Locate every Plasmodium falciparum-infected red blood cell.
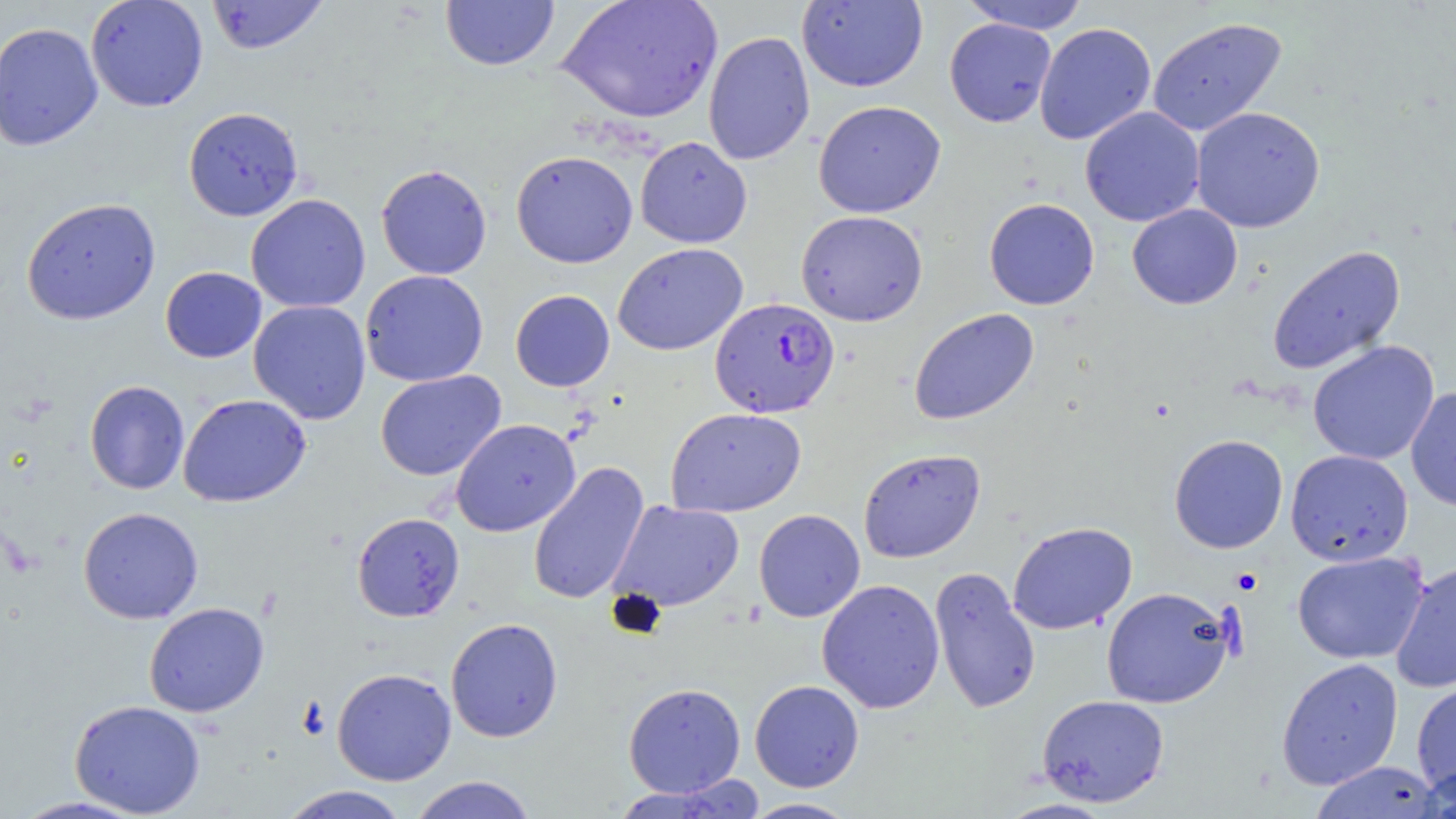
Approximate bounding boxes as [x1, y1, x2, y2] in pixels.
Plasmodium falciparum-infected red blood cells: [710, 297, 840, 418].

{
  "slide_level_diagnosis": "Plasmodium falciparum",
  "modality": "light microscopy",
  "stain": "May-Grünwald-Giemsa",
  "uninfected_red_blood_cell_locations": "approximate bounding boxes as [x1, y1, x2, y2] in pixels: [85, 0, 209, 112], [206, 0, 330, 55], [440, 0, 560, 71], [557, 0, 723, 124], [797, 1, 928, 92], [959, 1, 1090, 34], [1147, 16, 1288, 137], [944, 18, 1056, 128], [1, 22, 103, 151], [1034, 22, 1156, 145], [703, 30, 815, 166], [813, 100, 946, 218], [1190, 106, 1326, 233], [183, 107, 304, 221], [1079, 107, 1205, 227], [635, 136, 752, 248], [511, 150, 638, 268], [376, 164, 492, 279], [245, 194, 371, 313], [21, 197, 161, 325], [984, 198, 1100, 310], [1127, 204, 1243, 310], [795, 210, 928, 326], [613, 243, 748, 356], [1266, 244, 1405, 375], [160, 266, 266, 363], [360, 269, 488, 387], [510, 289, 615, 392], [248, 300, 371, 425], [908, 308, 1039, 425], [1307, 340, 1440, 465], [375, 369, 506, 481], [84, 380, 190, 495], [1406, 387, 1456, 512], [178, 393, 311, 507], [665, 407, 807, 517], [450, 418, 580, 537], [1169, 434, 1288, 553], [858, 448, 986, 563], [1285, 449, 1414, 566], [528, 461, 650, 606], [608, 500, 744, 612], [78, 506, 204, 624], [753, 509, 866, 622], [352, 512, 465, 621], [1007, 521, 1137, 635], [1292, 550, 1429, 664], [1390, 560, 1456, 695], [929, 567, 1041, 715], [816, 578, 945, 714], [1101, 587, 1236, 709], [143, 602, 269, 718], [445, 618, 563, 742], [1276, 657, 1404, 790], [332, 667, 456, 785], [1411, 678, 1456, 800], [749, 680, 864, 792], [623, 682, 746, 797], [1037, 694, 1170, 807], [69, 700, 206, 817], [1308, 760, 1446, 819], [1411, 764, 1456, 819], [408, 775, 538, 819], [608, 780, 763, 818], [278, 785, 412, 818], [8, 795, 152, 818], [741, 797, 859, 818], [998, 798, 1118, 818]",
  "preparation": "thin blood smear",
  "image_size": "1456×819 pixels",
  "field_of_view": "single",
  "magnification": "1000x",
  "platelet_locations": "approximate bounding boxes as [x1, y1, x2, y2] in pixels: [1231, 567, 1262, 594]"
}